Identify the blood parasite species.
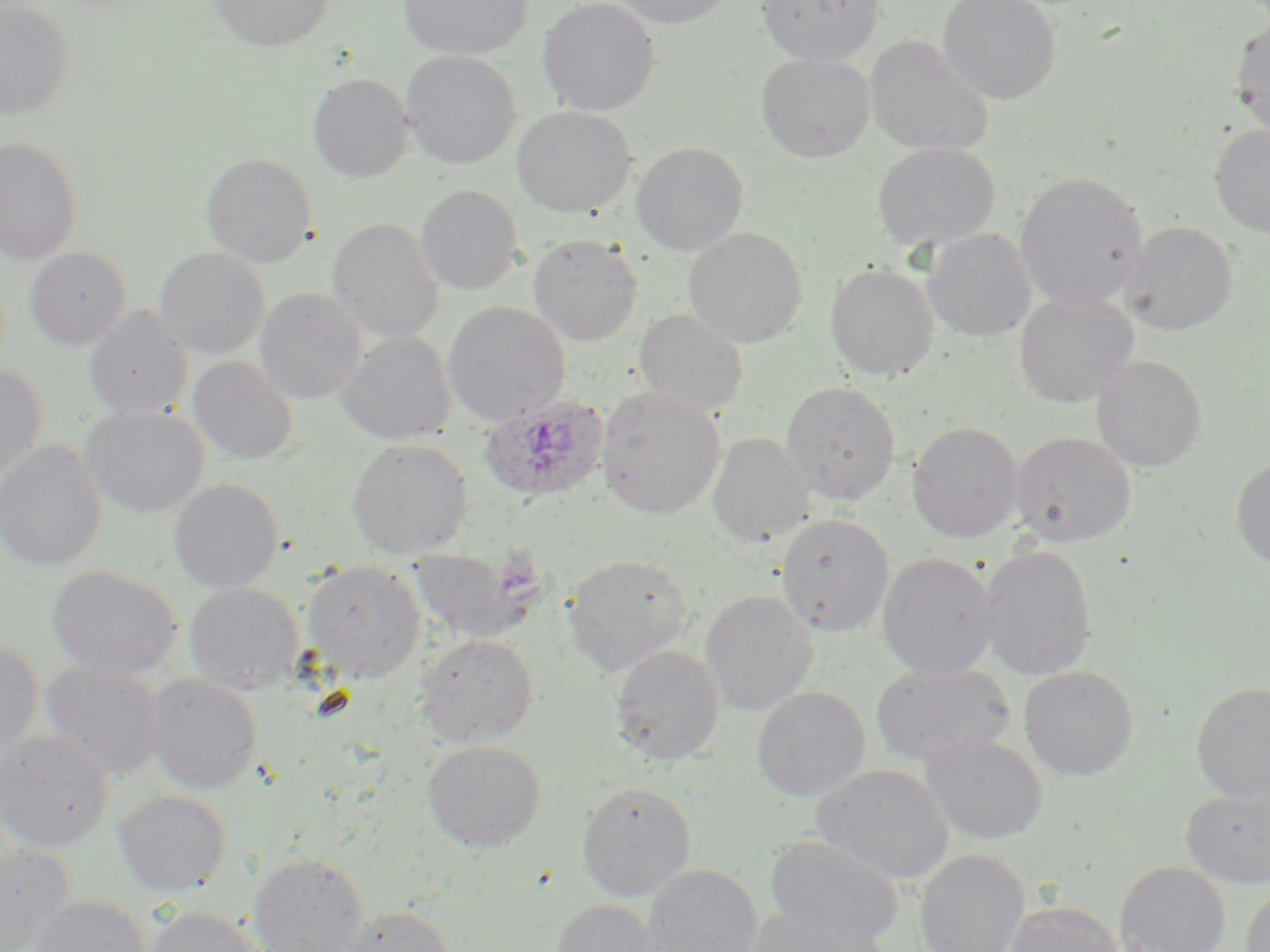
Plasmodium ovale.

Summary:
  - Coordinate format: approximate bounding boxes as [x1, y1, x2, y2] in pixels
  - Plasmodium ovale-infected red blood cell locations: [480, 396, 609, 506]
  - Uninfected red blood cell locations: [0, 0, 76, 121], [208, 0, 335, 52], [398, 0, 532, 60], [539, 0, 661, 117], [610, 0, 737, 28], [757, 0, 886, 64], [937, 0, 1061, 104], [1230, 17, 1270, 136], [865, 35, 995, 156], [400, 50, 521, 169], [756, 54, 875, 162], [306, 73, 415, 183], [511, 105, 637, 218], [1210, 122, 1270, 237], [0, 136, 83, 264], [631, 141, 748, 256], [872, 141, 1001, 254], [200, 153, 318, 268], [1015, 171, 1148, 311], [416, 184, 524, 295], [327, 218, 444, 343], [1121, 221, 1239, 335], [683, 227, 808, 348], [923, 228, 1036, 343], [527, 234, 643, 345], [23, 246, 131, 350], [154, 247, 270, 360], [825, 264, 939, 382], [255, 288, 367, 404], [1014, 291, 1139, 408], [442, 301, 571, 426], [84, 306, 193, 419], [634, 308, 749, 416], [336, 331, 456, 445], [1092, 355, 1207, 472], [188, 356, 299, 465], [0, 365, 48, 481], [780, 381, 901, 505], [596, 387, 725, 520], [80, 406, 210, 518], [907, 421, 1025, 543], [1010, 431, 1137, 547], [707, 433, 813, 548], [346, 438, 473, 559], [0, 440, 107, 572], [1231, 457, 1270, 571], [168, 478, 283, 593], [776, 513, 894, 637], [410, 542, 541, 643], [979, 545, 1097, 680], [877, 552, 1000, 679], [562, 553, 694, 675], [301, 561, 425, 682], [45, 564, 182, 681], [183, 582, 304, 693], [700, 590, 818, 716], [415, 633, 539, 748], [0, 639, 44, 762], [609, 645, 725, 765], [871, 660, 1015, 767], [40, 662, 165, 780], [1018, 665, 1139, 781], [144, 673, 263, 795], [1191, 682, 1270, 802], [751, 686, 871, 802], [0, 728, 114, 853], [920, 735, 1048, 844], [421, 740, 547, 852], [812, 763, 954, 884], [576, 782, 696, 902], [1181, 785, 1269, 888], [112, 790, 232, 896], [764, 834, 905, 949], [0, 846, 75, 951], [914, 849, 1030, 952], [248, 852, 369, 952], [1115, 860, 1230, 952], [641, 863, 763, 952], [1240, 882, 1269, 952], [29, 895, 151, 952], [548, 899, 663, 952], [1003, 902, 1126, 952], [143, 904, 260, 952], [340, 904, 456, 952], [741, 905, 893, 952]
  - Magnification: 1000x
  - Image size: 1270×952 pixels
  - Preparation: thin blood film
  - Modality: optical microscopy
  - Field of view: one of a larger specimen
  - Stain: May-Grünwald-Giemsa